Classify this cell by malaria status.
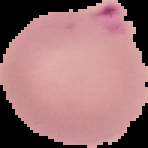

Parasitized.

From a thin blood film. Segmented cell region on a black background. Image is 148×148 pixels.